Assess this cell for malaria.
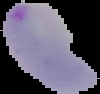

It is parasitized.

From a thin blood film. Image is 100×94 pixels. Cell region segmented out of the field of view; the surrounding area is masked to black.